State the blood parasite species.
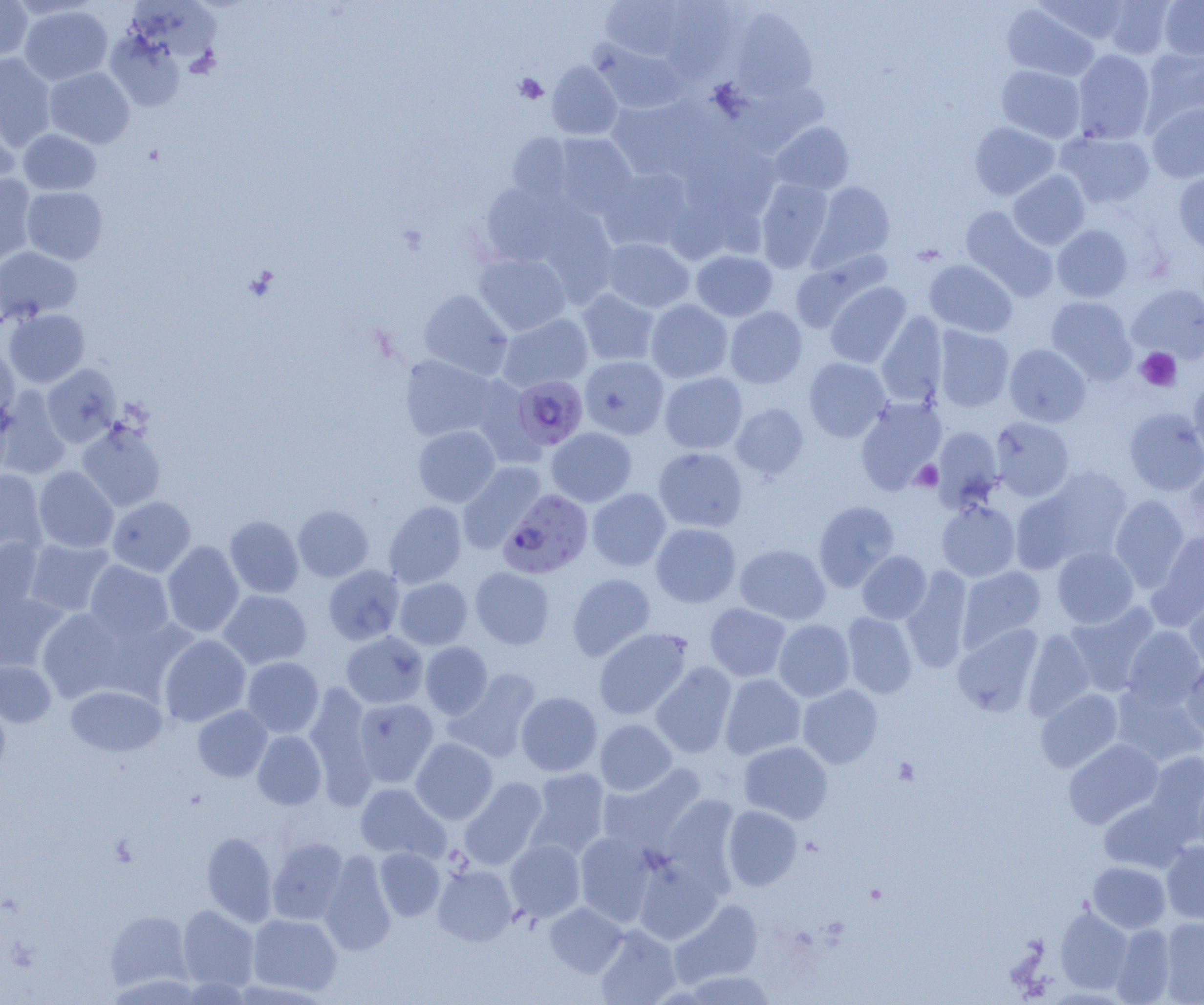

Plasmodium falciparum.

preparation = thin blood film
uninfected red blood cell locations = approximate bounding boxes as (x1,y1)-(x2,y2) corner pairs in pixels: (0,0)-(32,60), (600,0)-(687,60), (1036,0)-(1131,46), (1101,0)-(1175,58), (1158,0)-(1204,60), (659,1)-(741,79), (129,3)-(229,60), (1002,4)-(1099,81), (19,5)-(112,85), (731,8)-(817,100), (106,33)-(186,111), (592,40)-(689,115), (1141,47)-(1204,130), (1072,49)-(1155,144), (0,54)-(56,150), (547,61)-(622,139), (996,65)-(1086,142), (45,67)-(134,148), (605,97)-(714,181), (0,101)-(20,190), (1147,102)-(1204,183), (770,121)-(854,195), (969,122)-(1060,201), (18,129)-(101,195), (1057,130)-(1155,209), (507,133)-(574,204), (551,133)-(637,217), (600,168)-(692,252), (1008,170)-(1090,250), (1174,170)-(1204,254), (0,173)-(36,268), (755,178)-(833,272), (810,182)-(895,270), (480,183)-(573,267), (22,186)-(108,264), (960,207)-(1058,300), (1052,225)-(1133,302), (598,237)-(694,313), (0,247)-(82,322), (691,250)-(777,321), (473,253)-(571,336), (790,253)-(888,334), (924,259)-(1017,338), (825,282)-(911,368), (1127,284)-(1204,363), (418,289)-(513,380), (576,289)-(660,366), (1046,296)-(1136,383), (646,299)-(732,383), (724,306)-(807,388), (3,308)-(90,388), (877,311)-(948,408), (497,313)-(592,393), (933,326)-(1014,412), (0,341)-(19,429), (1004,343)-(1090,427), (399,355)-(499,442), (579,355)-(669,439), (804,357)-(890,442), (42,364)-(121,447), (659,372)-(747,454), (1189,379)-(1204,463), (0,387)-(71,479), (855,397)-(946,494), (731,403)-(809,479), (1124,407)-(1204,495), (990,417)-(1075,502), (77,421)-(166,512), (413,425)-(500,507), (932,426)-(1003,512), (546,427)-(636,507), (653,447)-(748,532), (457,462)-(546,552), (1180,463)-(1204,544), (34,466)-(118,553), (1022,466)-(1134,568), (0,469)-(47,556), (587,488)-(671,571), (1110,495)-(1190,590), (108,496)-(195,577), (813,500)-(899,592), (936,500)-(1020,582), (384,501)-(466,588), (293,505)-(373,582), (224,515)-(304,598), (651,523)-(741,607), (1151,530)-(1204,626), (0,537)-(46,621), (23,537)-(115,618), (162,541)-(244,637), (734,544)-(831,625), (1052,545)-(1139,629), (857,551)-(931,624), (85,560)-(174,642), (323,565)-(404,645), (958,566)-(1046,650), (470,567)-(554,649), (902,567)-(973,672), (567,573)-(655,660), (394,577)-(472,649), (0,590)-(65,672), (218,590)-(312,669), (1185,590)-(1204,672), (705,603)-(791,681), (1065,603)-(1160,696), (36,607)-(132,702), (842,612)-(917,699), (773,619)-(854,702), (952,624)-(1042,717), (1122,626)-(1204,710), (594,628)-(692,719), (1023,629)-(1094,722), (341,631)-(429,709), (159,634)-(251,726), (420,642)-(492,718), (242,657)-(324,737), (1182,658)-(1204,744), (0,659)-(56,728), (651,662)-(737,758), (445,669)-(541,763), (719,674)-(806,759), (1112,682)-(1204,768), (304,684)-(376,805), (797,684)-(883,768), (65,686)-(166,757), (1035,688)-(1123,773), (516,692)-(602,776), (0,696)-(10,780), (353,698)-(438,787), (192,705)-(272,782), (595,719)-(676,795), (252,731)-(326,809), (411,738)-(498,824), (1063,739)-(1163,829), (739,740)-(832,824), (1144,751)-(1204,837), (597,764)-(706,854), (526,767)-(610,859), (459,777)-(547,870), (1192,778)-(1204,859), (355,783)-(450,862), (1098,797)-(1193,873), (722,805)-(802,891), (202,831)-(277,926), (575,831)-(658,927), (268,837)-(348,925), (505,839)-(585,923), (1161,841)-(1204,924), (374,847)-(444,921), (319,851)-(396,956), (632,854)-(723,944), (1088,862)-(1170,932), (433,863)-(517,946), (670,899)-(764,987), (545,902)-(627,977), (178,905)-(259,992), (1056,906)-(1132,994), (105,909)-(192,993), (248,914)-(341,996), (1160,917)-(1204,1003), (1110,923)-(1176,1004), (594,925)-(680,1005), (684,970)-(778,1005)
Plasmodium falciparum-infected red blood cell locations = approximate bounding boxes as (x1,y1)-(x2,y2) corner pairs in pixels: (511,375)-(588,451), (498,489)-(593,579)
platelet locations = approximate bounding boxes as (x1,y1)-(x2,y2) corner pairs in pixels: (514,74)-(547,103), (1136,347)-(1182,391), (912,461)-(943,492), (892,757)-(919,786)
modality = optical microscopy
field of view = single
image size = 1204×1005 pixels
magnification = 1000x